Point out each Plasmodium parasite.
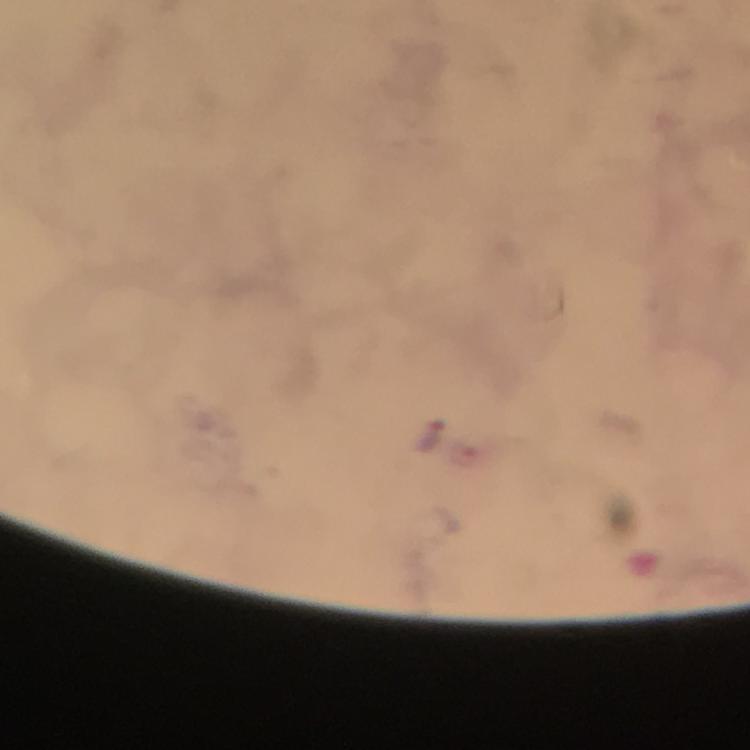
Approximate centers as [x, y] in pixels.
Plasmodium parasites: [436, 434].

immersion oil = applied
preparation = thick blood smear
context = from a diagnostic examination for malaria
stain = Giemsa
image size = 750×750 pixels
cropped from = a single field of view
magnification = 100x
capture = smartphone photograph through a microscope